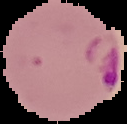

image_type: cell region segmented out of the field of view; surrounding area masked to black
preparation: thin blood film
image_size: 127×124 pixels
malaria_status: parasitized